State which parasite is depicted.
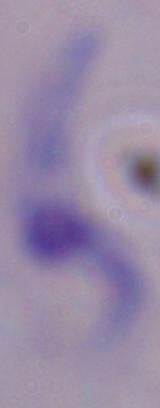
A trypanosome.

modality: micrograph
magnification: 1000x